Report the malaria status of this cell.
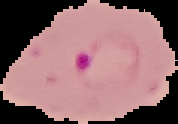
It is parasitized.

Image is 178×124 pixels. The area outside the segmented cell region is set to black. From a thin blood smear.